Comment on the morphology of the red blood cells.
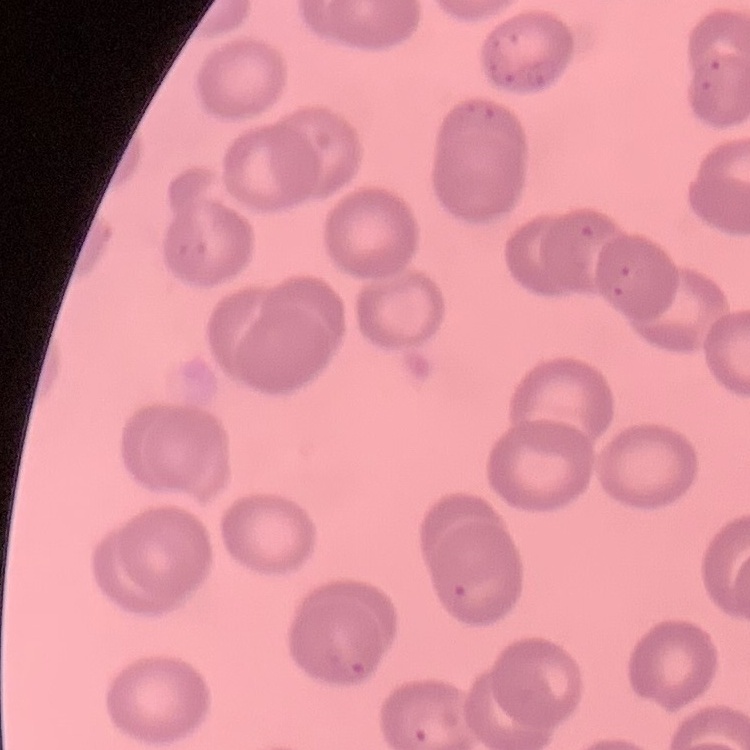
No rouleaux formation.

Square crop of a larger photomicrograph. Thin blood film. Stained with either Field's or Giemsa.